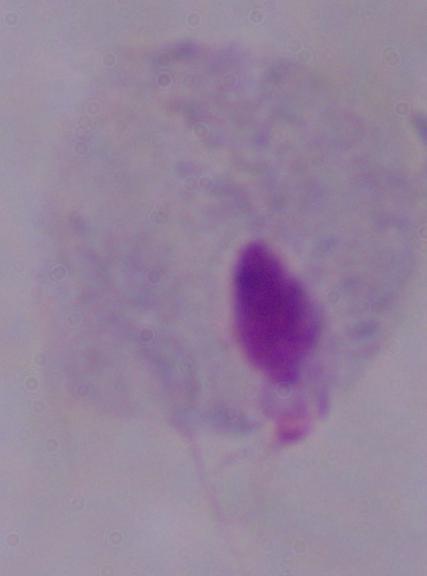

Summary:
  - Modality: photomicrograph
  - Identification: trichomonad
  - Magnification: 1000x